Describe the morphology of the erythrocytes.
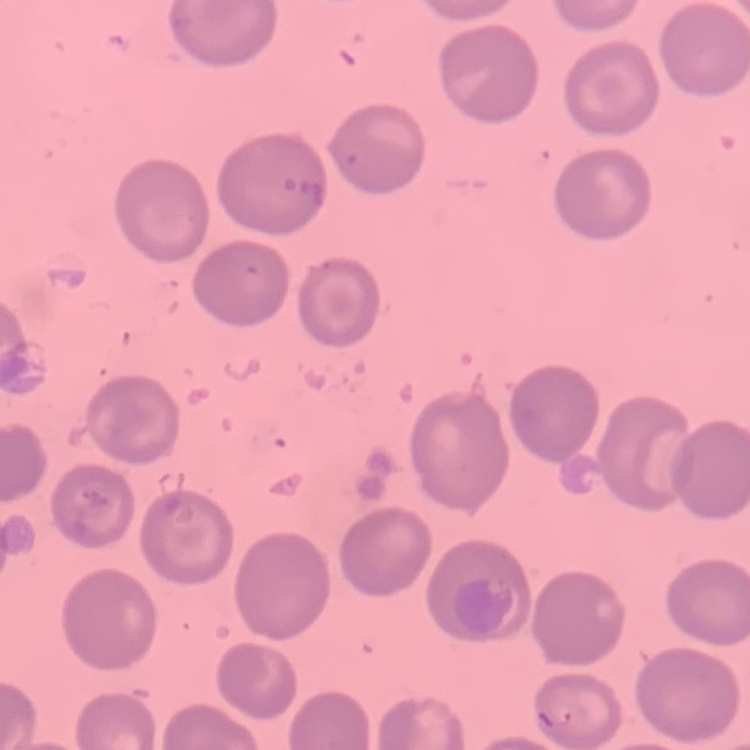

They show no rouleaux formation.

Summary:
  - Preparation: thin peripheral smear
  - Image type: one tile cut from a larger photomicrograph
  - Stain: Field's or Giemsa